Report the malaria status of this cell.
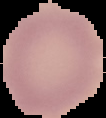

Uninfected.

Summary:
  - Preparation: thin blood film
  - Image size: 106×118 pixels
  - Image type: segmented cell region on a black background